Locate every blood parasite and identify its species.
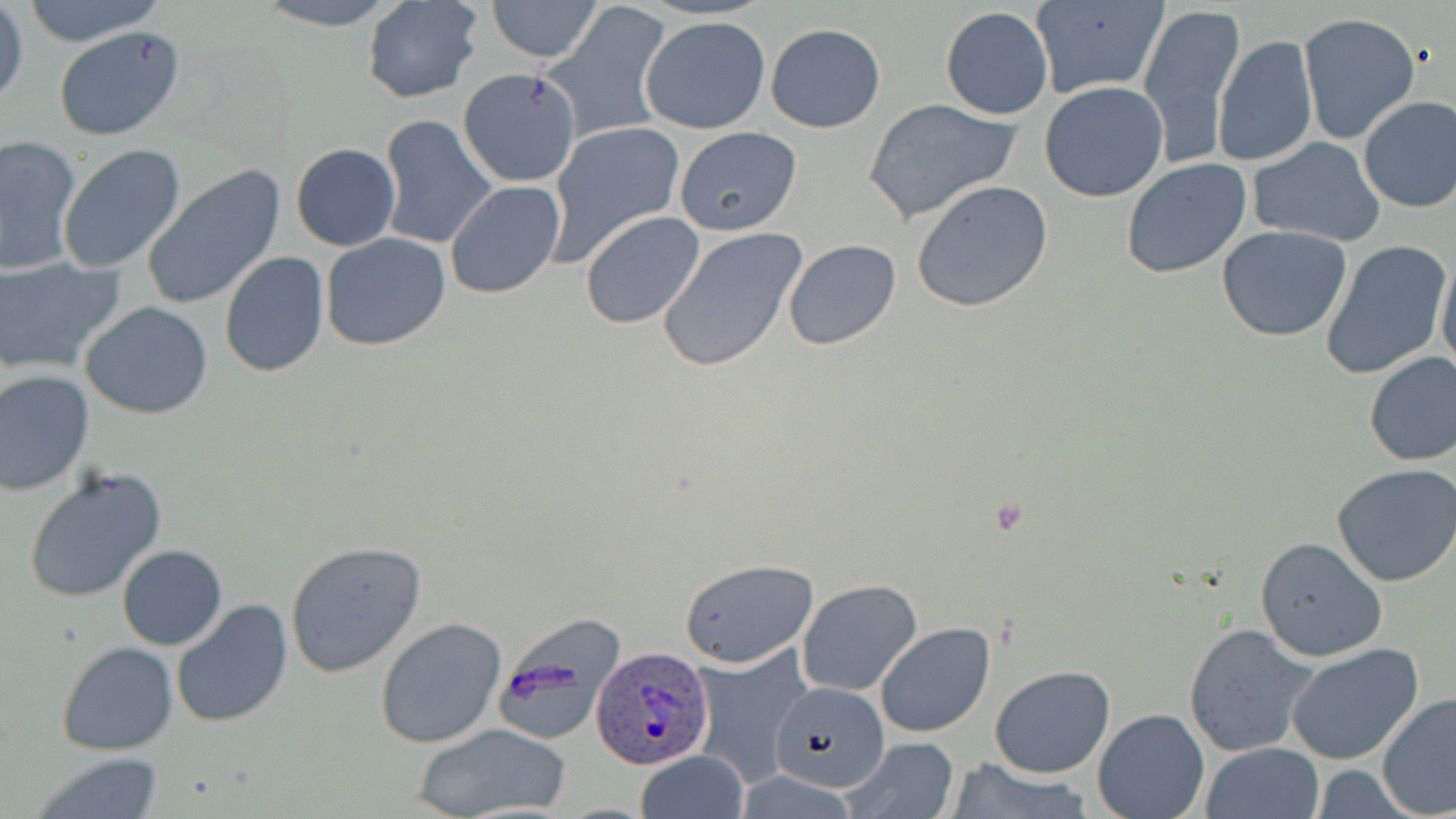
Approximate bounding boxes as (x1, y1, x2, y2) in pixels.
Plasmodium ovale-infected red blood cells: (591, 647, 714, 769).
No Plasmodium falciparum, Plasmodium malariae, Plasmodium vivax, Babesia divergens, or Trypanosoma brucei observed.

Summary:
  - Uninfected red blood cell locations: (17, 0, 167, 46), (251, 0, 403, 28), (486, 0, 603, 62), (1031, 0, 1168, 100), (361, 1, 484, 104), (1139, 1, 1245, 164), (1, 3, 27, 109), (540, 4, 675, 142), (939, 6, 1054, 120), (1296, 11, 1421, 146), (639, 16, 770, 135), (764, 23, 886, 133), (53, 27, 184, 142), (1212, 35, 1318, 170), (458, 68, 582, 188), (1039, 82, 1169, 202), (1357, 95, 1456, 213), (863, 97, 1022, 225), (379, 114, 497, 251), (546, 121, 685, 262), (674, 126, 802, 236), (1, 135, 81, 273), (1247, 136, 1387, 247), (291, 142, 400, 251), (57, 145, 185, 274), (1122, 157, 1253, 279), (142, 164, 286, 310), (445, 180, 565, 299), (911, 180, 1054, 312), (580, 211, 707, 329), (1216, 226, 1353, 344), (655, 227, 806, 373), (321, 233, 452, 351), (1319, 237, 1452, 380), (782, 239, 902, 351), (219, 251, 329, 378), (1437, 252, 1456, 379), (0, 256, 125, 374), (80, 301, 215, 419), (1362, 351, 1456, 466), (0, 369, 96, 494), (1331, 463, 1456, 588), (23, 466, 167, 604), (1254, 536, 1388, 662), (283, 540, 426, 678), (116, 544, 227, 650), (680, 559, 817, 667), (798, 579, 922, 696), (170, 599, 294, 728), (374, 616, 507, 749), (876, 622, 993, 738), (1183, 623, 1319, 759), (57, 640, 180, 754), (1284, 643, 1428, 767), (692, 647, 815, 781), (990, 665, 1115, 779), (770, 679, 889, 792), (1377, 692, 1456, 819), (1092, 709, 1211, 819), (410, 723, 572, 819), (838, 737, 961, 818), (1203, 743, 1323, 819), (634, 751, 750, 819), (29, 752, 167, 819), (940, 759, 1099, 819)
  - Slide-level diagnosis: Plasmodium ovale
  - Modality: optical microscopy
  - Preparation: thin blood smear
  - Stain: May-Grünwald-Giemsa
  - Magnification: 1000x
  - Image size: 1456×819 pixels
  - Field of view: single